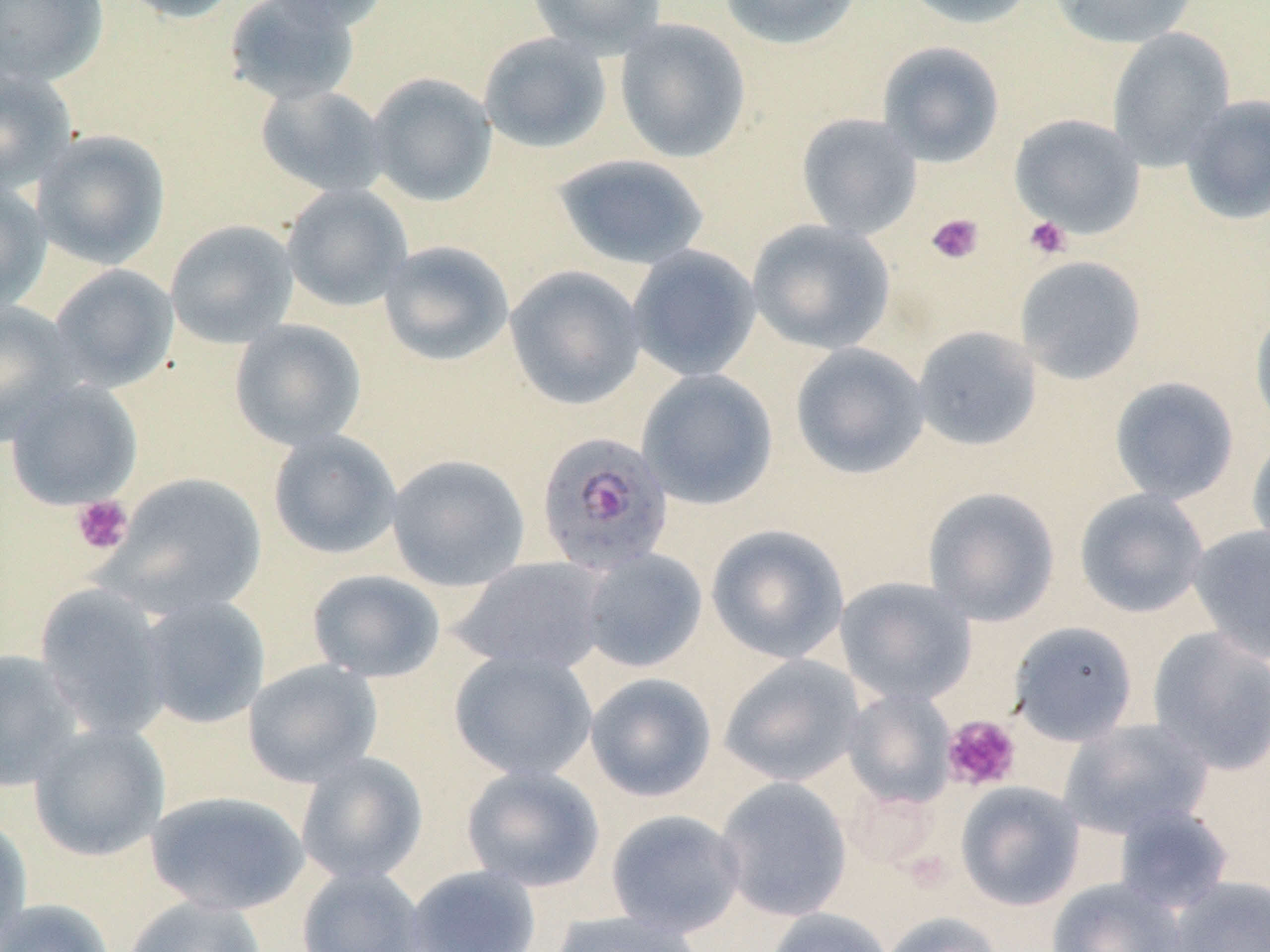

Summary:
  - Coordinate format: approximate bounding boxes as named x1/y1/x2/y2 corners in pixels
  - Uninfected red blood cell locations: (x1=0, y1=0, x2=110, y2=88), (x1=116, y1=0, x2=242, y2=23), (x1=223, y1=0, x2=362, y2=107), (x1=262, y1=0, x2=391, y2=31), (x1=528, y1=0, x2=667, y2=57), (x1=719, y1=0, x2=863, y2=50), (x1=899, y1=0, x2=1040, y2=29), (x1=1047, y1=0, x2=1198, y2=49), (x1=614, y1=18, x2=751, y2=164), (x1=1107, y1=27, x2=1236, y2=172), (x1=478, y1=32, x2=613, y2=154), (x1=876, y1=41, x2=1006, y2=168), (x1=0, y1=66, x2=78, y2=196), (x1=366, y1=72, x2=497, y2=207), (x1=255, y1=83, x2=390, y2=198), (x1=1180, y1=94, x2=1270, y2=225), (x1=796, y1=113, x2=923, y2=239), (x1=1009, y1=113, x2=1146, y2=239), (x1=31, y1=130, x2=171, y2=269), (x1=552, y1=154, x2=711, y2=270), (x1=0, y1=181, x2=52, y2=315), (x1=281, y1=184, x2=413, y2=311), (x1=747, y1=219, x2=895, y2=355), (x1=165, y1=220, x2=299, y2=348), (x1=378, y1=241, x2=514, y2=367), (x1=626, y1=244, x2=762, y2=382), (x1=1014, y1=256, x2=1147, y2=385), (x1=47, y1=264, x2=179, y2=393), (x1=504, y1=265, x2=647, y2=410), (x1=0, y1=303, x2=82, y2=445), (x1=1250, y1=303, x2=1270, y2=435), (x1=228, y1=319, x2=367, y2=451), (x1=912, y1=325, x2=1043, y2=452), (x1=790, y1=342, x2=930, y2=479), (x1=636, y1=368, x2=778, y2=510), (x1=1109, y1=376, x2=1239, y2=505), (x1=3, y1=379, x2=144, y2=511), (x1=267, y1=429, x2=403, y2=560), (x1=1247, y1=433, x2=1270, y2=559), (x1=386, y1=454, x2=530, y2=592), (x1=107, y1=472, x2=268, y2=618), (x1=922, y1=487, x2=1061, y2=626), (x1=1074, y1=488, x2=1209, y2=618), (x1=705, y1=523, x2=849, y2=664), (x1=1187, y1=524, x2=1270, y2=661), (x1=577, y1=548, x2=708, y2=673), (x1=450, y1=556, x2=611, y2=675), (x1=306, y1=569, x2=446, y2=683), (x1=834, y1=576, x2=977, y2=706), (x1=34, y1=583, x2=173, y2=741), (x1=136, y1=594, x2=271, y2=730), (x1=1009, y1=621, x2=1139, y2=746), (x1=1146, y1=627, x2=1270, y2=775), (x1=0, y1=649, x2=85, y2=792), (x1=448, y1=649, x2=598, y2=782), (x1=718, y1=654, x2=866, y2=787), (x1=242, y1=659, x2=383, y2=788), (x1=584, y1=672, x2=717, y2=802), (x1=841, y1=688, x2=958, y2=808), (x1=1058, y1=717, x2=1213, y2=840), (x1=28, y1=722, x2=171, y2=862), (x1=295, y1=752, x2=429, y2=885), (x1=460, y1=764, x2=605, y2=892), (x1=714, y1=776, x2=852, y2=922), (x1=955, y1=781, x2=1085, y2=910), (x1=143, y1=789, x2=311, y2=916), (x1=1112, y1=803, x2=1235, y2=913), (x1=605, y1=809, x2=747, y2=938), (x1=0, y1=815, x2=33, y2=947), (x1=402, y1=864, x2=542, y2=952), (x1=296, y1=865, x2=428, y2=952), (x1=1165, y1=874, x2=1270, y2=952), (x1=1046, y1=877, x2=1186, y2=952), (x1=122, y1=895, x2=268, y2=952), (x1=0, y1=898, x2=117, y2=952), (x1=763, y1=907, x2=895, y2=952), (x1=547, y1=910, x2=707, y2=952), (x1=878, y1=911, x2=1005, y2=952)
  - Plasmodium falciparum-infected red blood cell locations: (x1=535, y1=431, x2=674, y2=576)
  - Platelet locations: (x1=925, y1=212, x2=985, y2=265), (x1=1023, y1=216, x2=1072, y2=260), (x1=71, y1=495, x2=134, y2=555), (x1=941, y1=715, x2=1022, y2=793)
  - Slide-level diagnosis: Plasmodium falciparum
  - Field of view: single
  - Stain: May-Grünwald-Giemsa
  - Magnification: 1000x
  - Preparation: thin blood film
  - Modality: light microscopy
  - Image size: 1270×952 pixels